Locate every malaria parasite.
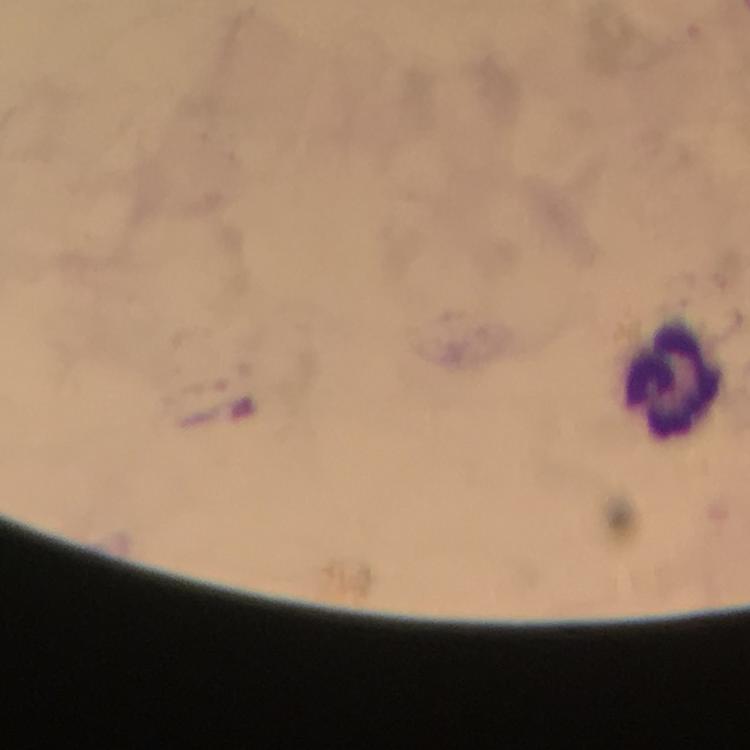

No malaria parasites seen.

cropped from = a single field of view
image size = 750×750 pixels
leukocyte locations = approximate centers as (x, y) in pixels: (669, 381)
preparation = thick blood film
stain = Giemsa
capture = smartphone mounted on the microscope
magnification = 100x
immersion oil = applied
context = from a malaria diagnostic workup